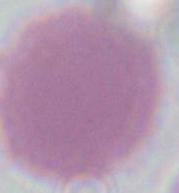 Captured at 1000x magnification. Micrograph. A red blood cell is shown.